Locate every blood parasite and identify its species.
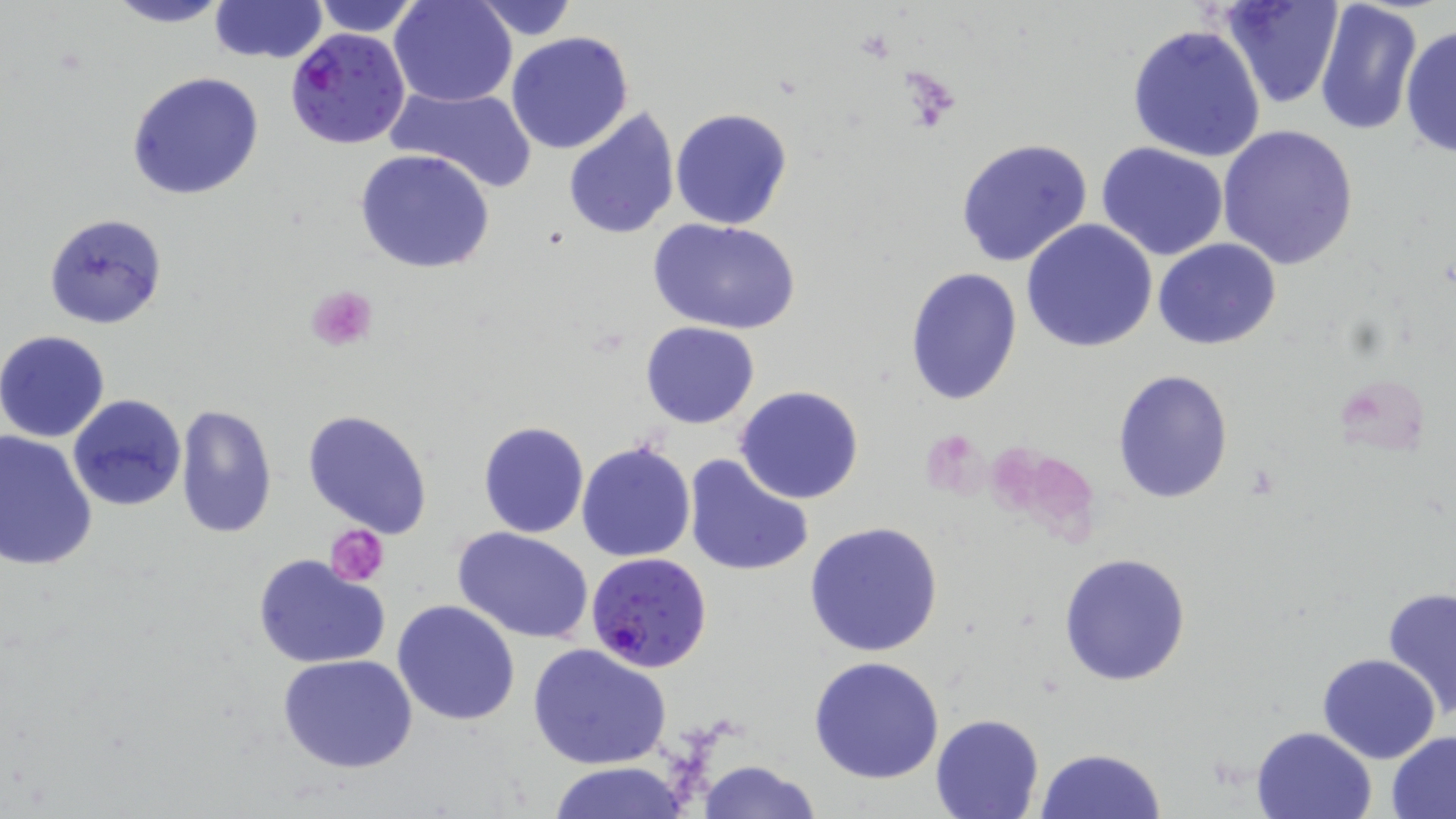

Approximate bounding boxes as named x1/y1/x2/y2 corners in pixels.
Plasmodium falciparum-infected red blood cells: (x1=286, y1=29, x2=409, y2=150), (x1=585, y1=551, x2=713, y2=673).
No Plasmodium ovale, Plasmodium malariae, Plasmodium vivax, Babesia divergens, or Trypanosoma brucei observed.

Uninfected red blood cell locations: (x1=103, y1=0, x2=233, y2=27), (x1=208, y1=0, x2=327, y2=65), (x1=390, y1=0, x2=517, y2=107), (x1=467, y1=0, x2=579, y2=41), (x1=1219, y1=0, x2=1343, y2=109), (x1=1314, y1=0, x2=1424, y2=138), (x1=309, y1=1, x2=428, y2=36), (x1=1126, y1=24, x2=1267, y2=163), (x1=1402, y1=24, x2=1455, y2=162), (x1=506, y1=31, x2=634, y2=156), (x1=127, y1=71, x2=263, y2=200), (x1=386, y1=84, x2=537, y2=194), (x1=562, y1=107, x2=681, y2=240), (x1=670, y1=107, x2=794, y2=231), (x1=1216, y1=125, x2=1359, y2=270), (x1=956, y1=137, x2=1096, y2=269), (x1=1096, y1=143, x2=1229, y2=260), (x1=354, y1=149, x2=496, y2=274), (x1=44, y1=213, x2=166, y2=329), (x1=650, y1=218, x2=802, y2=335), (x1=1021, y1=220, x2=1158, y2=354), (x1=1153, y1=239, x2=1280, y2=350), (x1=904, y1=268, x2=1023, y2=406), (x1=642, y1=322, x2=760, y2=429), (x1=0, y1=330, x2=110, y2=442), (x1=1113, y1=369, x2=1234, y2=502), (x1=733, y1=384, x2=865, y2=505), (x1=68, y1=395, x2=189, y2=511), (x1=175, y1=403, x2=278, y2=539), (x1=302, y1=408, x2=435, y2=540), (x1=478, y1=421, x2=588, y2=538), (x1=1, y1=429, x2=99, y2=573), (x1=577, y1=439, x2=696, y2=563), (x1=681, y1=455, x2=813, y2=577), (x1=803, y1=520, x2=943, y2=658), (x1=454, y1=528, x2=595, y2=643), (x1=1059, y1=553, x2=1192, y2=688), (x1=252, y1=554, x2=392, y2=670), (x1=1381, y1=586, x2=1456, y2=722), (x1=391, y1=599, x2=520, y2=726), (x1=527, y1=643, x2=671, y2=769), (x1=277, y1=652, x2=419, y2=775), (x1=1316, y1=653, x2=1441, y2=763), (x1=809, y1=655, x2=944, y2=784), (x1=931, y1=712, x2=1045, y2=817), (x1=1251, y1=725, x2=1379, y2=819), (x1=1387, y1=731, x2=1456, y2=816), (x1=1035, y1=746, x2=1167, y2=819), (x1=694, y1=759, x2=823, y2=818), (x1=545, y1=765, x2=695, y2=819). Platelet locations: (x1=305, y1=285, x2=378, y2=352), (x1=328, y1=526, x2=388, y2=585). Slide-level diagnosis: Plasmodium falciparum. Single field of view. 1000x magnification. Thin blood film. Image is 1456×819 pixels. Optical microscopy. May-Grünwald-Giemsa stain.